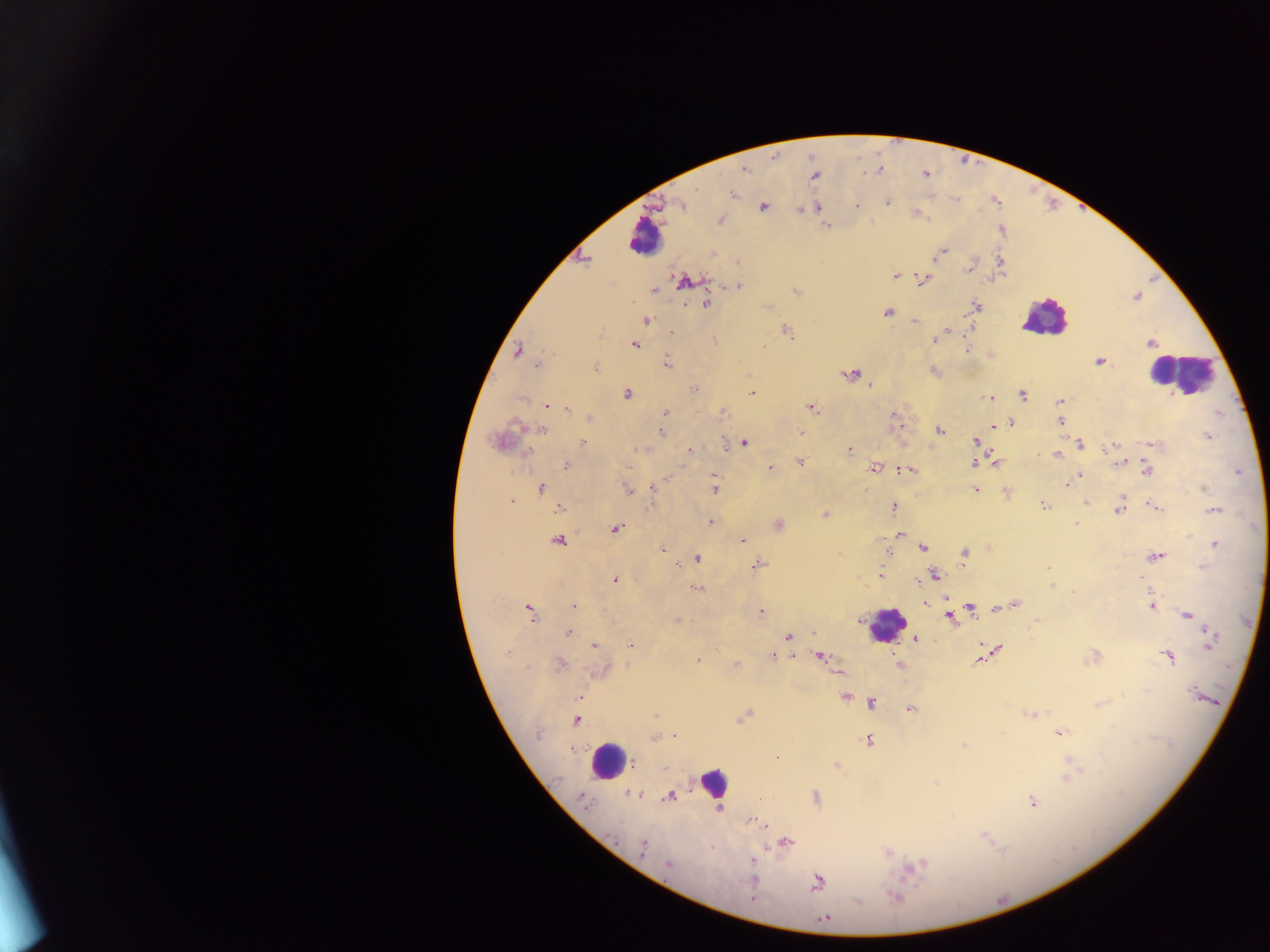
{
  "field_of_view": "single",
  "capture": "mobile-phone photograph through a microscope",
  "country": "Ghana",
  "image_size": "1270×952 pixels",
  "preparation": "thick blood film",
  "malaria_parasite_locations": "approximate centers as [x, y] in pixels: [744, 168], [879, 169], [814, 176], [733, 194], [887, 202], [680, 204], [857, 204], [763, 207], [818, 207], [801, 209], [720, 220], [826, 225], [942, 252], [935, 257], [584, 260], [970, 267], [895, 276], [683, 280], [923, 280], [738, 286], [653, 291], [796, 291], [1137, 296], [705, 305], [976, 305], [887, 312], [647, 320], [915, 321], [946, 330], [671, 332], [787, 332], [934, 339], [715, 340], [1151, 342], [635, 344], [966, 349], [518, 351], [1100, 362], [667, 363], [536, 366], [596, 368], [933, 370], [852, 374], [869, 387], [694, 388], [627, 393], [752, 393], [1022, 395], [991, 397], [1060, 401], [546, 405], [811, 407], [568, 409], [665, 413], [724, 413], [894, 414], [590, 418], [1011, 422], [1060, 422], [516, 425], [994, 426], [543, 430], [939, 430], [661, 432], [800, 432], [1207, 436], [976, 441], [744, 442], [582, 443], [1081, 444], [1152, 444], [1114, 445], [640, 450], [849, 450], [688, 451], [1057, 454], [1037, 455], [801, 462], [1120, 462], [973, 463], [995, 463], [566, 465], [770, 468], [874, 469], [905, 469], [1148, 471], [1080, 474], [713, 475], [1067, 485], [653, 486], [541, 488], [1203, 489], [715, 490], [628, 491], [976, 491], [1006, 492], [511, 501], [1086, 502], [1044, 506], [559, 508], [893, 508], [1156, 508], [1119, 509], [1215, 510], [825, 515], [711, 522], [1076, 524], [779, 525], [616, 529], [901, 534], [743, 539], [558, 540], [1215, 544], [662, 548], [923, 548], [965, 554], [1157, 556], [697, 559], [677, 564], [758, 564], [1203, 566], [1049, 568], [880, 575], [935, 575], [614, 580], [919, 584], [1051, 586], [697, 588], [1073, 593], [948, 599], [925, 604], [1014, 605], [1152, 605], [573, 606], [970, 608], [997, 608], [529, 610], [762, 612], [1187, 614], [950, 616], [677, 620], [1037, 620], [568, 634], [1210, 635], [788, 637], [915, 639], [629, 644], [594, 645], [1210, 645], [998, 648], [507, 653], [772, 656], [819, 657], [1094, 657], [1169, 657], [699, 660], [979, 660], [561, 664], [736, 665], [527, 667], [602, 670], [1145, 690], [1197, 694], [581, 697], [844, 697], [872, 703], [910, 709], [1031, 714], [655, 715], [743, 717], [576, 721], [1062, 732], [537, 734], [654, 738], [868, 740], [963, 746], [1070, 762], [836, 765], [1068, 777], [935, 783], [632, 794], [669, 797], [815, 797], [583, 799], [1032, 802], [756, 821], [760, 823], [788, 841], [642, 847], [753, 859], [668, 865], [915, 866], [752, 880], [817, 882], [895, 897], [753, 899], [824, 918]",
  "leukocyte_locations": "approximate centers as [x, y] in pixels: [644, 238], [1044, 318], [1180, 373], [887, 624], [607, 760], [714, 783]"
}